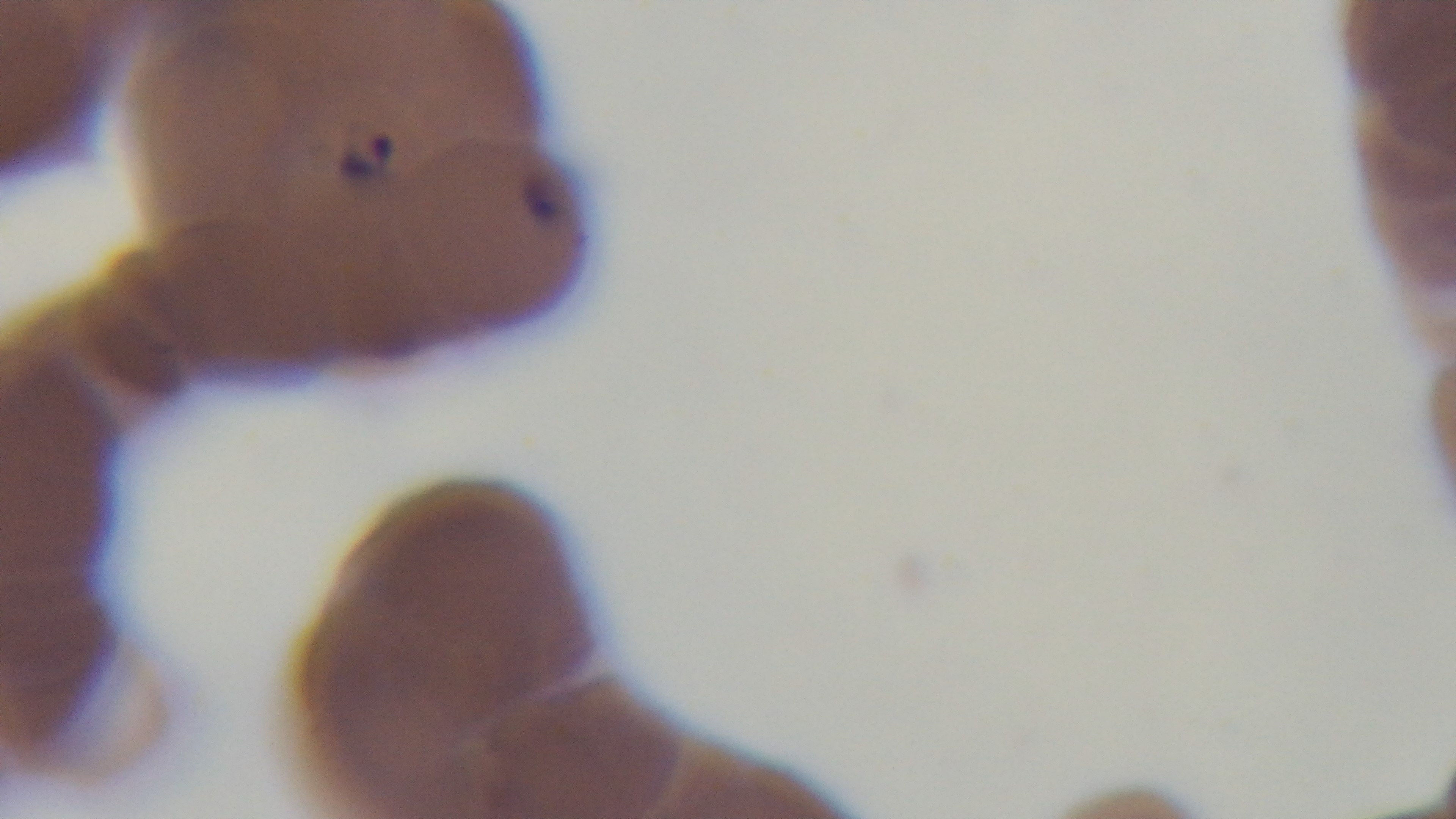
{
  "capture": "mounted 4K digital camera",
  "objective": "100x oil immersion",
  "modality": "light microscopy",
  "preparation": "thin",
  "stain": "Giemsa",
  "field_of_view": "single",
  "malaria_status": "positive"
}